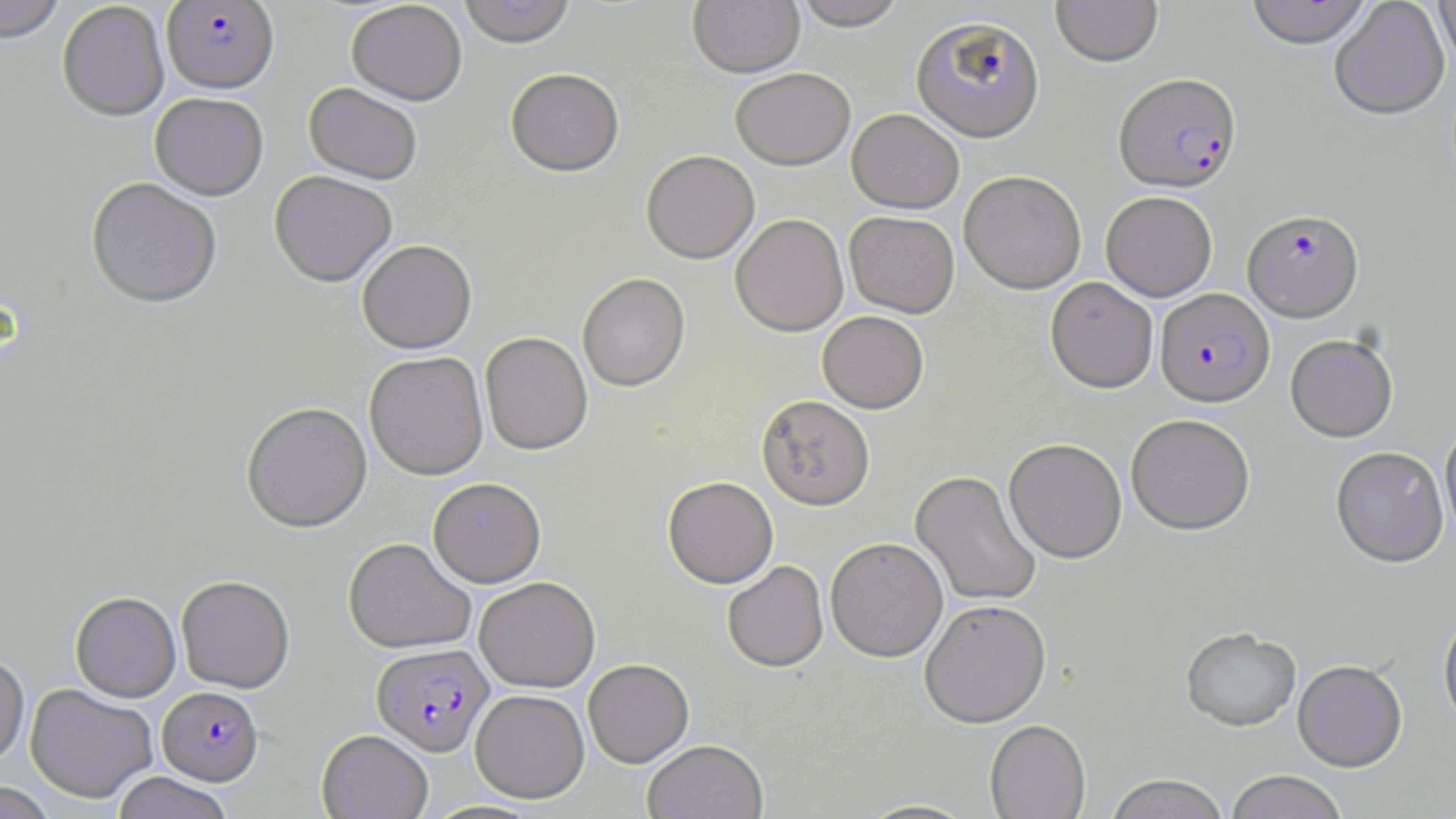

Summary:
  - Coordinate format: approximate bounding boxes as (x1, y1, x2, y2) in pixels
  - Uninfected red blood cell locations: (0, 0, 65, 45), (458, 0, 576, 51), (688, 0, 805, 81), (793, 0, 908, 34), (1051, 0, 1163, 67), (1244, 0, 1374, 49), (1329, 0, 1449, 122), (1434, 0, 1456, 73), (346, 2, 467, 108), (57, 3, 169, 123), (506, 71, 624, 181), (731, 71, 854, 173), (303, 84, 421, 187), (150, 95, 268, 202), (846, 110, 964, 216), (641, 153, 759, 267), (959, 173, 1086, 295), (269, 174, 396, 290), (86, 180, 222, 311), (1101, 193, 1217, 302), (844, 213, 959, 319), (731, 216, 849, 339), (357, 242, 477, 356), (577, 275, 691, 394), (1045, 278, 1158, 394), (817, 313, 929, 415), (480, 333, 593, 457), (1285, 336, 1398, 444), (364, 353, 488, 481), (756, 397, 875, 513), (241, 404, 373, 534), (1126, 416, 1255, 537), (1440, 424, 1456, 543), (1004, 440, 1127, 564), (1331, 448, 1449, 570), (910, 472, 1042, 607), (663, 479, 778, 591), (428, 480, 546, 589), (343, 539, 476, 655), (826, 539, 947, 665), (722, 563, 829, 674), (176, 577, 295, 693), (474, 578, 601, 693), (70, 593, 181, 703), (920, 603, 1052, 731), (1438, 611, 1456, 738), (1182, 630, 1301, 735), (0, 653, 29, 768), (583, 660, 694, 769), (1292, 663, 1408, 775), (25, 684, 157, 804), (470, 691, 589, 804), (985, 722, 1091, 819), (317, 731, 432, 819), (642, 742, 768, 819), (111, 772, 234, 819), (1226, 772, 1347, 819), (1105, 776, 1230, 819), (0, 782, 56, 819), (856, 799, 981, 819)
  - Plasmodium falciparum-infected red blood cell locations: (161, 1, 279, 96), (911, 19, 1045, 145), (1114, 74, 1241, 194), (1243, 212, 1364, 324), (1155, 290, 1275, 410), (371, 644, 494, 758), (158, 687, 264, 786)
  - Slide-level diagnosis: Plasmodium falciparum
  - Magnification: 1000x
  - Stain: May-Grünwald-Giemsa
  - Modality: optical microscopy
  - Field of view: one of a larger specimen
  - Preparation: thin blood smear
  - Image size: 1456×819 pixels